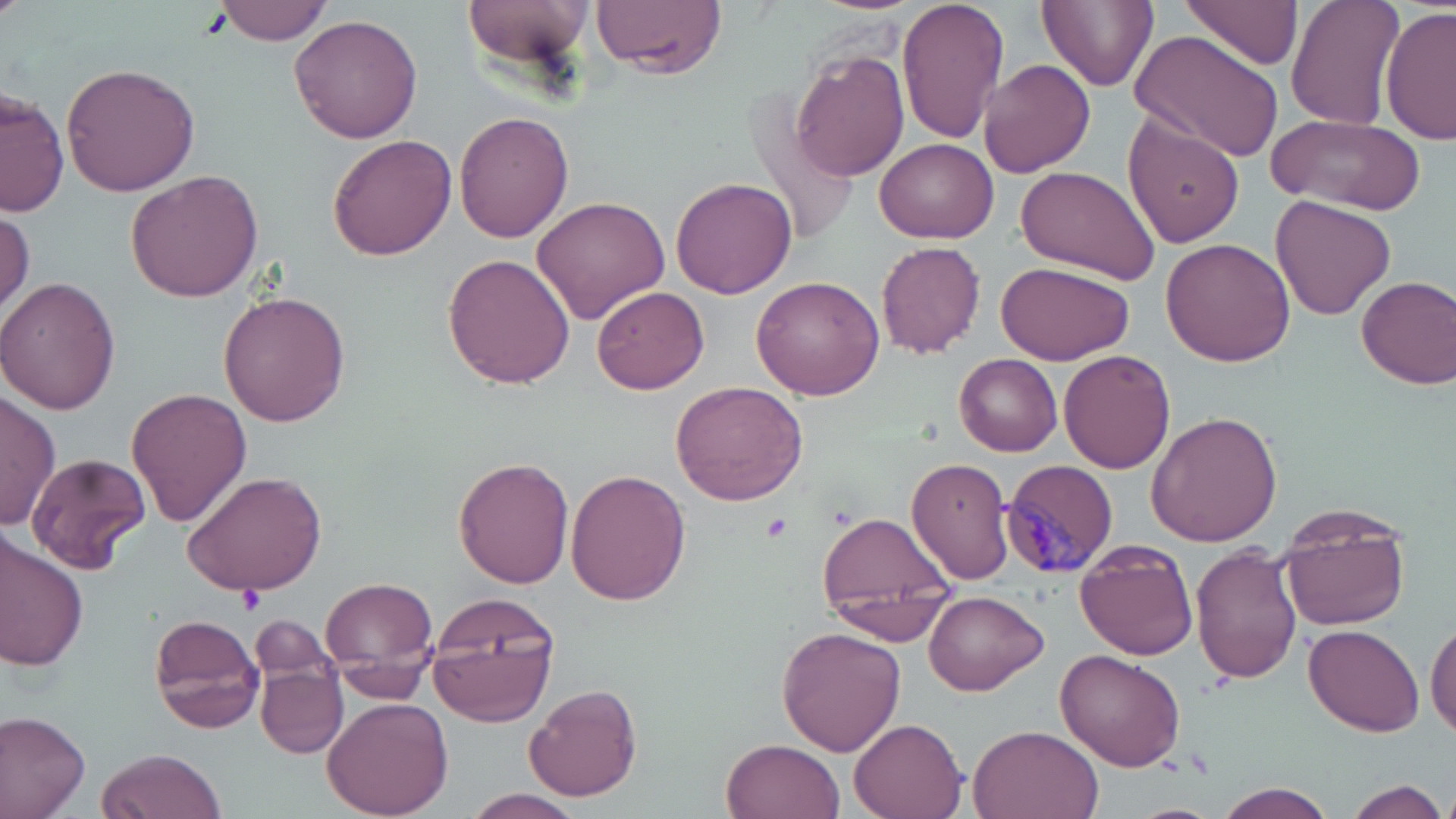

slide-level diagnosis = Plasmodium malariae
field of view = single
stain = May-Grünwald-Giemsa
magnification = 1000x
Plasmodium malariae-infected red blood cell locations = approximate bounding boxes as named x1/y1/x2/y2 corners in pixels: (x1=1002, y1=458, x2=1119, y2=577)
uninfected red blood cell locations = approximate bounding boxes as named x1/y1/x2/y2 corners in pixels: (x1=462, y1=0, x2=595, y2=74), (x1=594, y1=0, x2=726, y2=78), (x1=896, y1=0, x2=1010, y2=145), (x1=1039, y1=0, x2=1157, y2=91), (x1=1180, y1=0, x2=1305, y2=71), (x1=1286, y1=0, x2=1405, y2=131), (x1=212, y1=1, x2=336, y2=45), (x1=1378, y1=6, x2=1455, y2=148), (x1=289, y1=15, x2=423, y2=142), (x1=1131, y1=29, x2=1285, y2=164), (x1=791, y1=49, x2=910, y2=181), (x1=977, y1=60, x2=1095, y2=177), (x1=62, y1=62, x2=200, y2=196), (x1=741, y1=85, x2=859, y2=249), (x1=1, y1=91, x2=66, y2=218), (x1=455, y1=111, x2=575, y2=245), (x1=1122, y1=112, x2=1247, y2=249), (x1=1268, y1=113, x2=1425, y2=217), (x1=327, y1=135, x2=457, y2=261), (x1=873, y1=138, x2=1000, y2=241), (x1=1013, y1=166, x2=1161, y2=285), (x1=126, y1=170, x2=263, y2=301), (x1=672, y1=177, x2=797, y2=298), (x1=531, y1=195, x2=670, y2=323), (x1=1272, y1=196, x2=1396, y2=319), (x1=0, y1=203, x2=33, y2=323), (x1=1159, y1=238, x2=1297, y2=367), (x1=876, y1=241, x2=986, y2=358), (x1=442, y1=254, x2=575, y2=390), (x1=995, y1=259, x2=1132, y2=364), (x1=1356, y1=274, x2=1456, y2=388), (x1=751, y1=276, x2=883, y2=400), (x1=0, y1=278, x2=122, y2=415), (x1=592, y1=285, x2=710, y2=395), (x1=218, y1=292, x2=350, y2=426), (x1=1059, y1=350, x2=1175, y2=475), (x1=954, y1=355, x2=1062, y2=455), (x1=670, y1=380, x2=807, y2=505), (x1=0, y1=386, x2=58, y2=533), (x1=126, y1=387, x2=253, y2=525), (x1=1144, y1=410, x2=1283, y2=547), (x1=27, y1=453, x2=151, y2=574), (x1=453, y1=457, x2=574, y2=589), (x1=907, y1=458, x2=1014, y2=584), (x1=566, y1=469, x2=691, y2=606), (x1=181, y1=470, x2=329, y2=596), (x1=1276, y1=507, x2=1411, y2=631), (x1=816, y1=511, x2=960, y2=643), (x1=0, y1=535, x2=87, y2=673), (x1=1074, y1=538, x2=1200, y2=660), (x1=1190, y1=544, x2=1304, y2=684), (x1=321, y1=578, x2=438, y2=685), (x1=427, y1=591, x2=565, y2=724), (x1=922, y1=591, x2=1047, y2=695), (x1=148, y1=612, x2=265, y2=734), (x1=251, y1=615, x2=345, y2=701), (x1=1427, y1=616, x2=1456, y2=737), (x1=1304, y1=623, x2=1425, y2=736), (x1=777, y1=626, x2=907, y2=756), (x1=1056, y1=649, x2=1185, y2=771), (x1=257, y1=664, x2=348, y2=757), (x1=522, y1=681, x2=643, y2=802), (x1=323, y1=697, x2=455, y2=819), (x1=0, y1=710, x2=91, y2=819), (x1=847, y1=719, x2=967, y2=819), (x1=968, y1=724, x2=1104, y2=819), (x1=722, y1=738, x2=845, y2=819), (x1=98, y1=747, x2=226, y2=818), (x1=1340, y1=780, x2=1451, y2=819), (x1=1211, y1=781, x2=1336, y2=819), (x1=461, y1=790, x2=585, y2=818)
image size = 1456×819 pixels
modality = light microscopy
platelet locations = approximate bounding boxes as named x1/y1/x2/y2 corners in pixels: (x1=762, y1=512, x2=792, y2=542), (x1=239, y1=585, x2=262, y2=611)
preparation = thin blood film